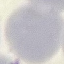
Summary:
  - Result: no malaria parasites detected
  - Image type: cell patch, automatically extracted from a larger field of view and resized to 64 × 64 pixels
  - Stain: Giemsa
  - Preparation: thin blood smear
  - Capture: smartphone camera at the microscope eyepiece